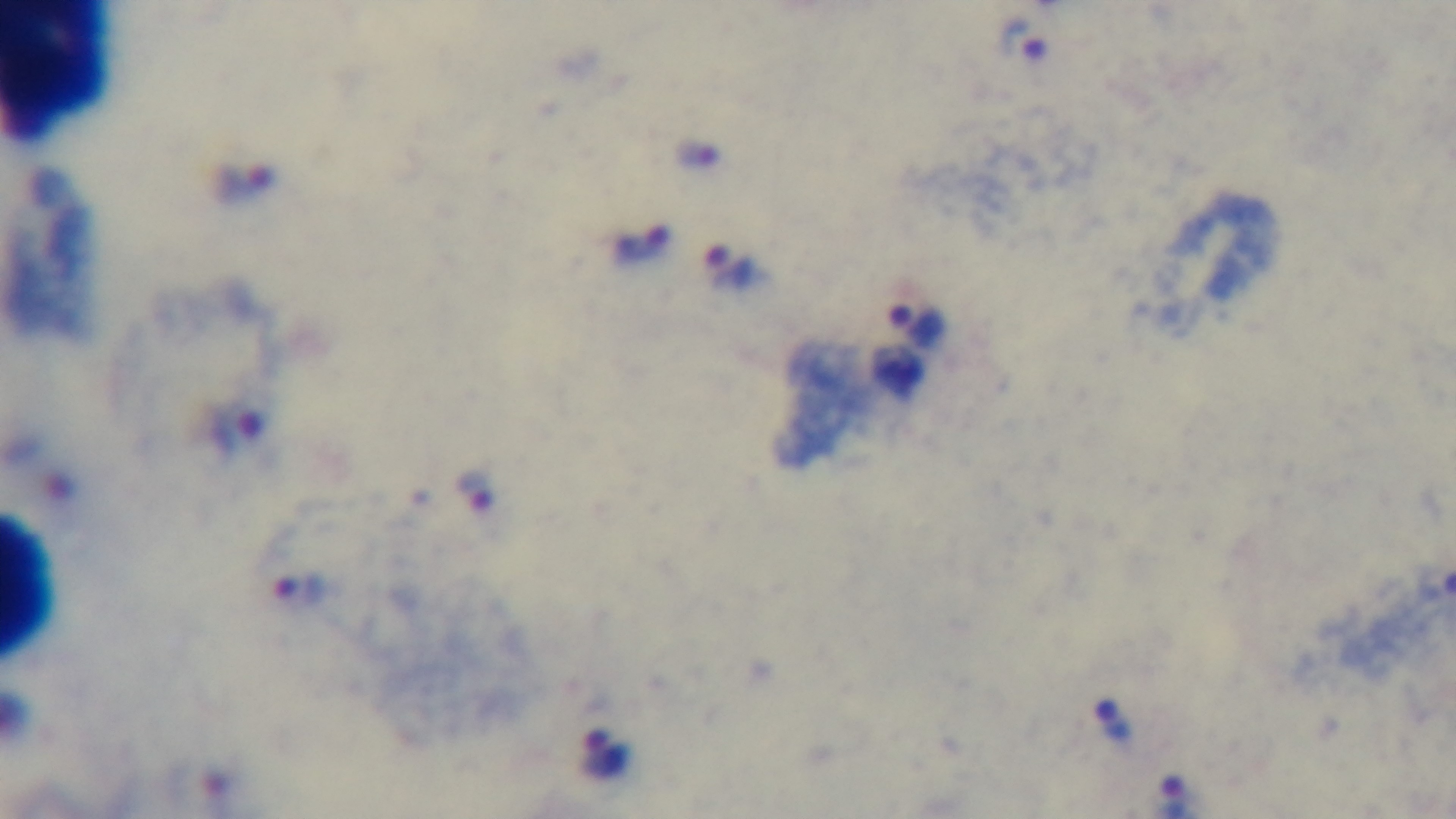
capture = mounted 4K digital camera
field of view = one from the slide
malaria status = positive
stain = Giemsa
modality = light microscopy
preparation = thick smear
objective = 100x oil immersion